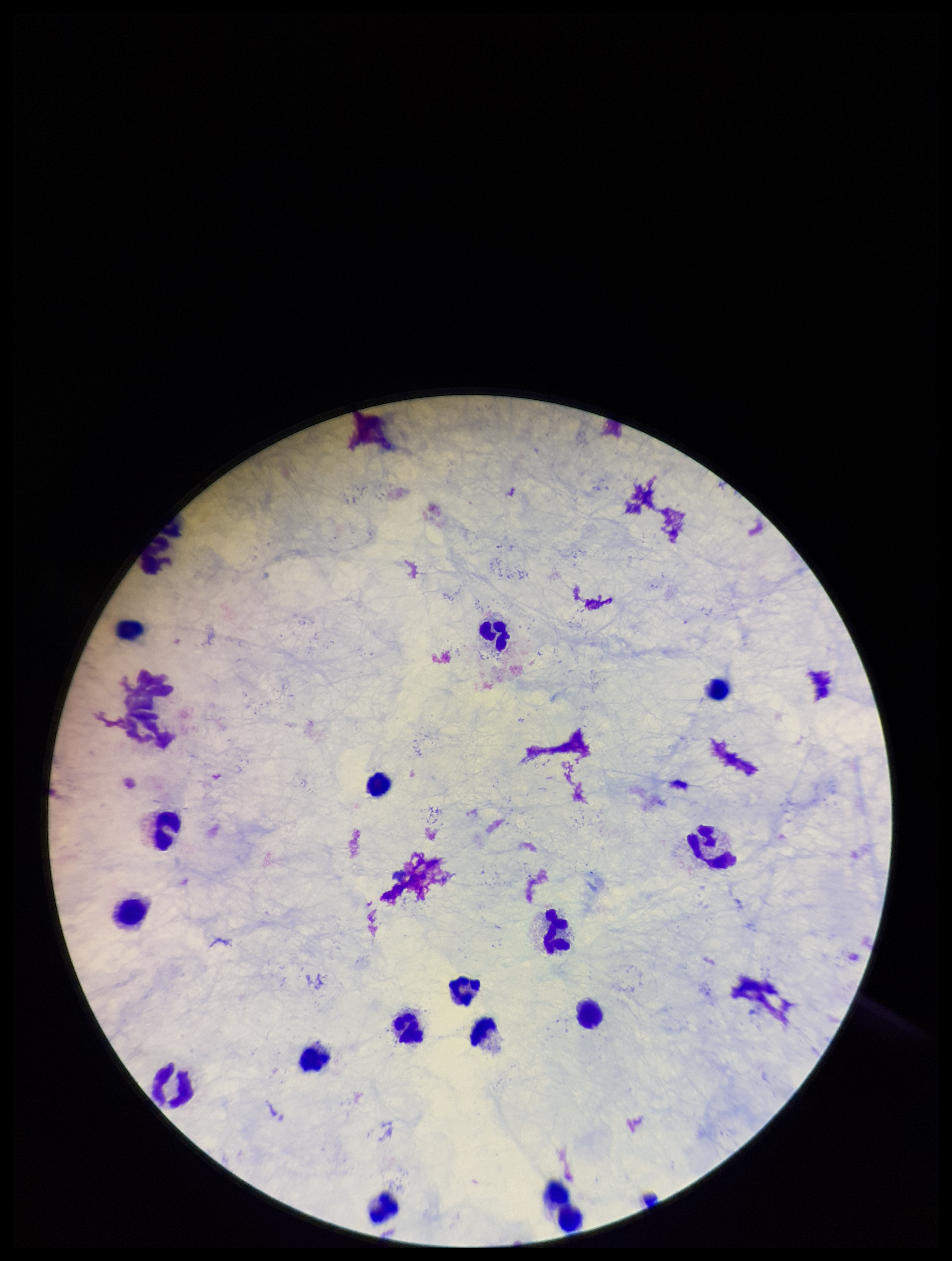
Summary:
  - Field of view: single
  - Preparation: thick
  - Parasite count: 0
  - Capture: smartphone photograph through the microscope eyepiece
  - Plasmodium parasites: none seen
  - Patient malaria status: negative
  - Image size: 952×1261 pixels
  - Stain: Giemsa
  - Leukocyte count: 16